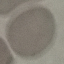
Malaria status: uninfected. Thin blood film. Acquired by smartphone through the microscope eyepiece. Giemsa-stained preparation. Automatically extracted cell patch, resized to 64 × 64 pixels.